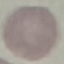

Summary:
  - Result: no malaria parasites seen
  - Capture: smartphone through the microscope eyepiece
  - Preparation: thin blood smear
  - Image type: cell patch, automatically extracted from a larger field of view and resized to 64 × 64 pixels
  - Stain: Giemsa